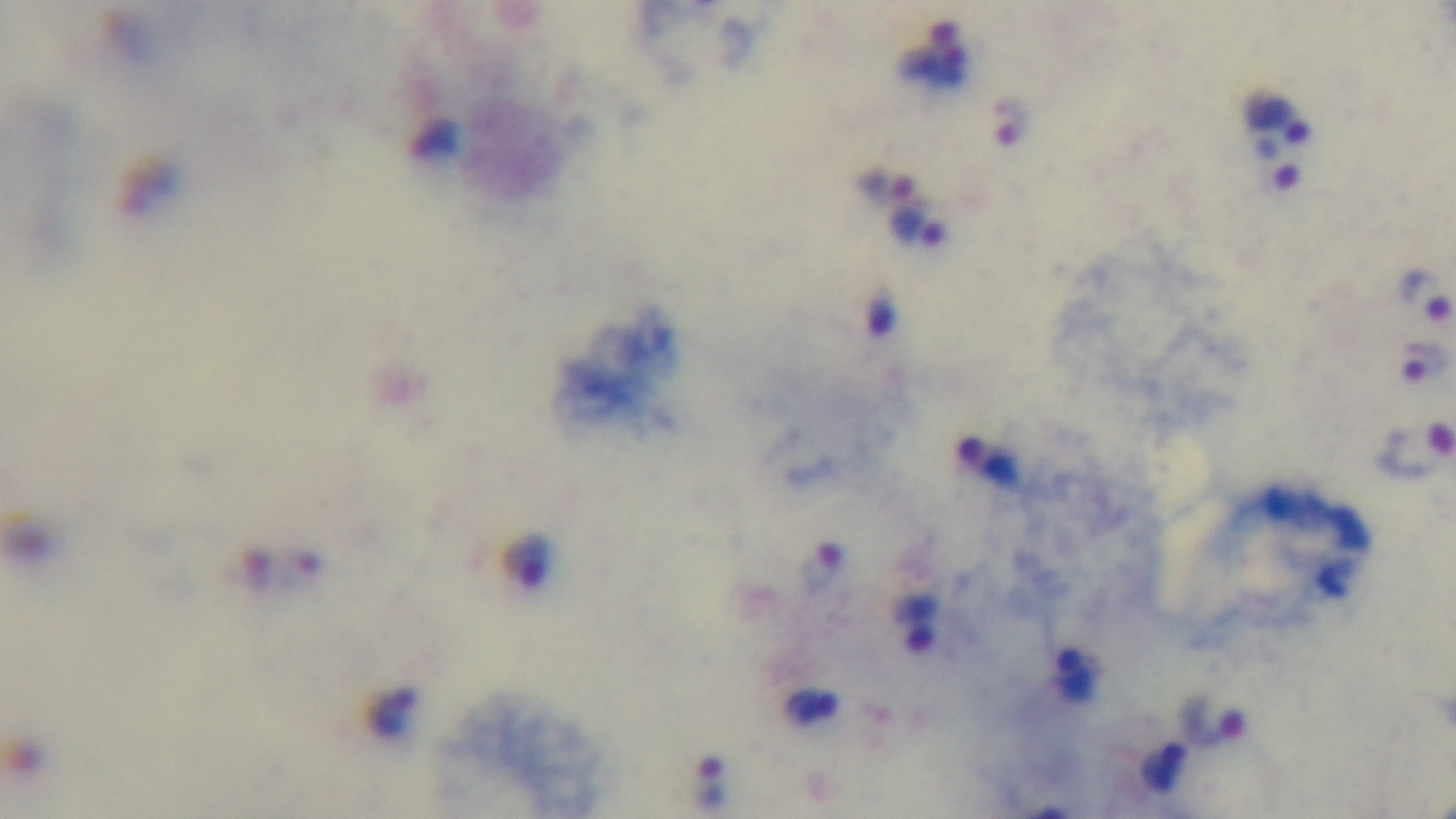
preparation: thick smear
stain: Giemsa
malaria_status: positive
capture: mounted 4K digital camera
modality: light microscopy
field_of_view: single
objective: 100x oil immersion